Give the position of every malaria parasite.
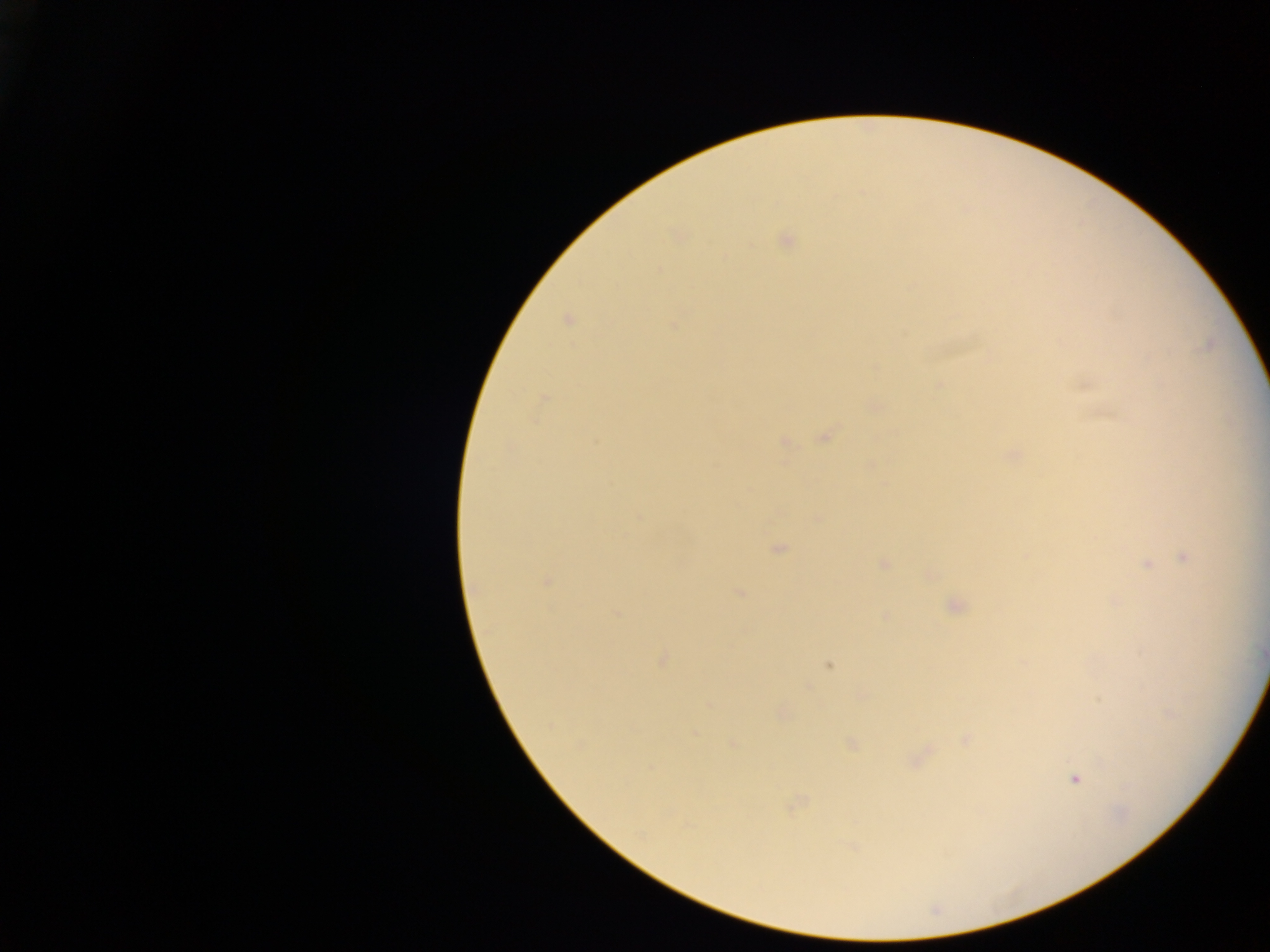

Approximate centers as [x, y] in pixels.
Malaria parasites: [675, 236], [786, 240], [725, 256], [660, 271], [566, 320], [673, 324], [1085, 386], [543, 399], [875, 406], [825, 437], [785, 442], [1013, 455], [638, 516], [818, 517], [778, 548], [1184, 557], [883, 564], [1146, 564], [546, 581], [739, 593], [1115, 602], [955, 606], [616, 613], [884, 617], [662, 659], [828, 666], [709, 705], [782, 712], [694, 732], [966, 739], [852, 744], [734, 745], [1075, 780], [795, 804], [686, 825], [850, 846].

capture = mobile-phone photograph through a microscope
country = Ghana
image size = 1270×952 pixels
field of view = single
preparation = thick blood film